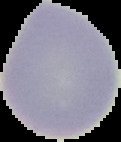

image size = 121×142 pixels
image type = segmented cell region with the area outside set to black
preparation = thin blood smear
result = no malaria parasites seen